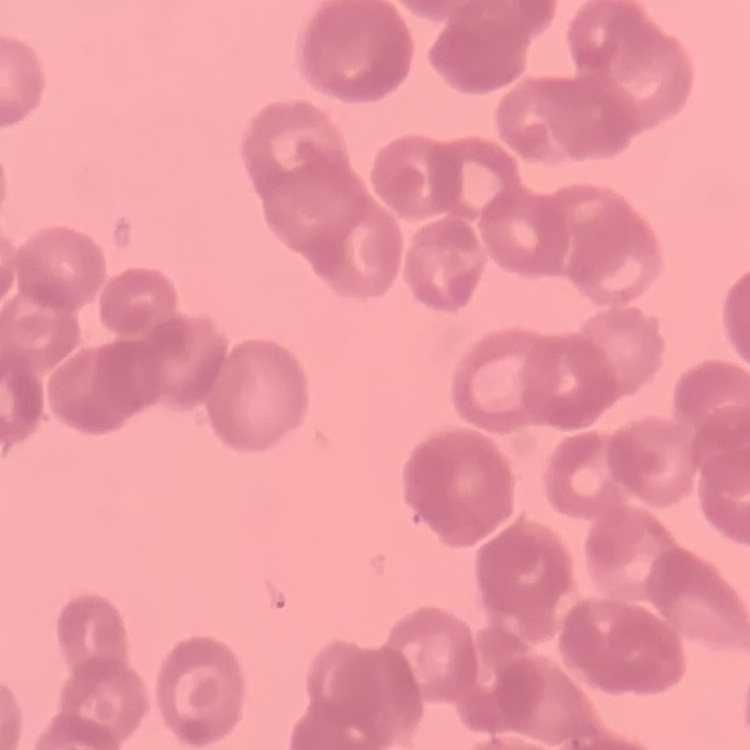

red blood cell morphology = rouleaux formation
preparation = thin blood film
image type = one tile cut from a larger photomicrograph
stain = Field's or Giemsa